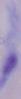
A trypanosome is seen. Captured at 1000x magnification. Micrograph.